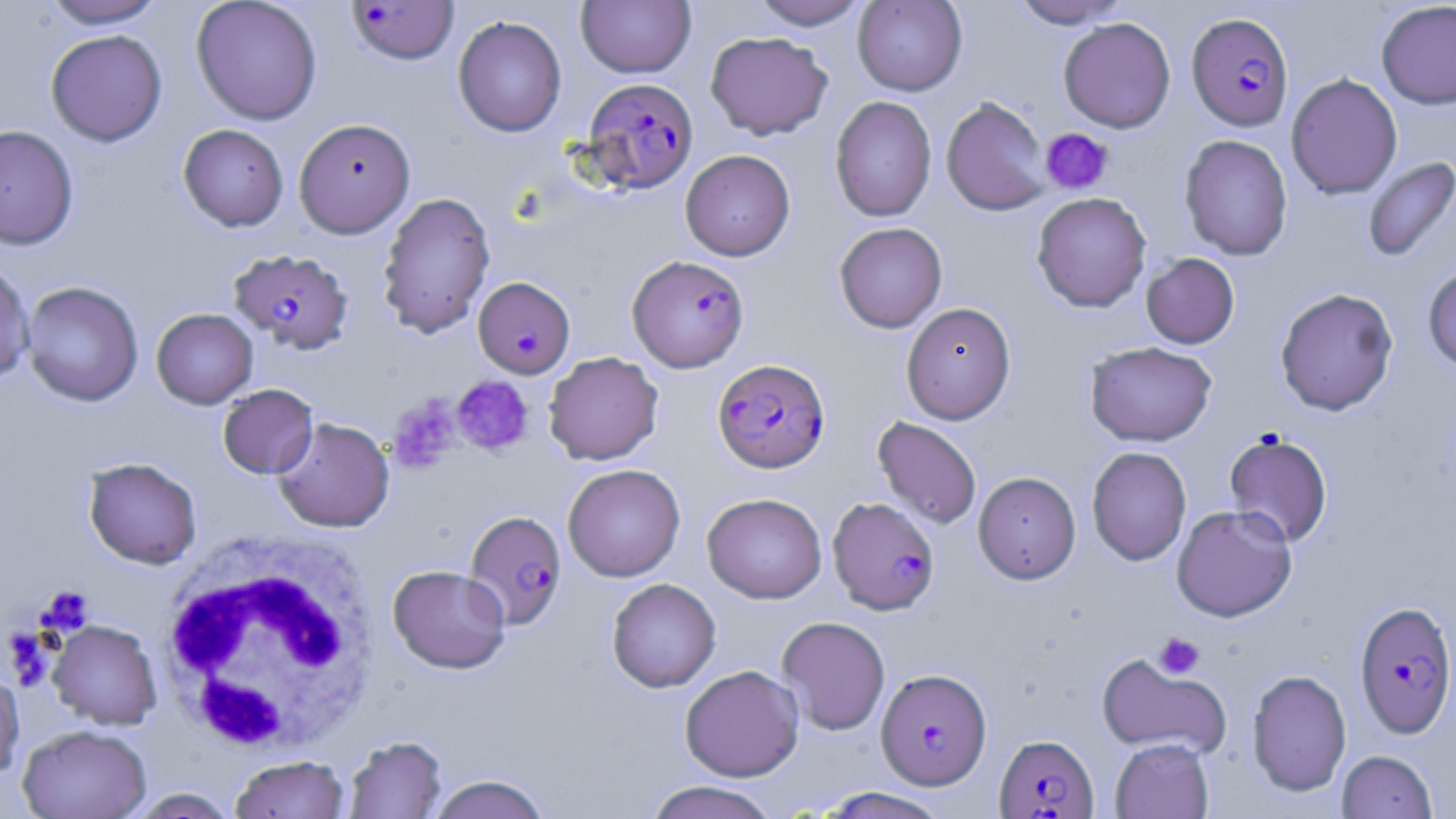

Approximate bounding boxes as named x1/y1/x2/y2 corners in pixels. White blood cell locations: (x1=156, y1=532, x2=383, y2=756). Platelet locations: (x1=1041, y1=128, x2=1113, y2=195), (x1=451, y1=375, x2=534, y2=457), (x1=391, y1=397, x2=462, y2=471), (x1=40, y1=586, x2=94, y2=634), (x1=1154, y1=633, x2=1204, y2=679). Uninfected red blood cell locations: (x1=42, y1=0, x2=168, y2=29), (x1=191, y1=0, x2=323, y2=125), (x1=749, y1=0, x2=869, y2=30), (x1=1010, y1=0, x2=1131, y2=29), (x1=576, y1=1, x2=696, y2=78), (x1=852, y1=1, x2=968, y2=96), (x1=1375, y1=1, x2=1456, y2=109), (x1=452, y1=15, x2=567, y2=137), (x1=1058, y1=17, x2=1176, y2=133), (x1=46, y1=29, x2=167, y2=146), (x1=705, y1=31, x2=833, y2=140), (x1=1285, y1=73, x2=1403, y2=200), (x1=829, y1=96, x2=937, y2=222), (x1=941, y1=96, x2=1053, y2=216), (x1=294, y1=118, x2=416, y2=238), (x1=178, y1=124, x2=289, y2=231), (x1=0, y1=125, x2=79, y2=250), (x1=1179, y1=134, x2=1293, y2=261), (x1=680, y1=149, x2=795, y2=261), (x1=1362, y1=156, x2=1456, y2=263), (x1=377, y1=191, x2=496, y2=338), (x1=1031, y1=191, x2=1151, y2=312), (x1=834, y1=223, x2=947, y2=334), (x1=1141, y1=253, x2=1240, y2=349), (x1=0, y1=260, x2=35, y2=385), (x1=1422, y1=263, x2=1456, y2=372), (x1=21, y1=280, x2=144, y2=406), (x1=1275, y1=287, x2=1399, y2=416), (x1=901, y1=302, x2=1016, y2=424), (x1=151, y1=308, x2=258, y2=409), (x1=1085, y1=341, x2=1217, y2=446), (x1=544, y1=352, x2=664, y2=465), (x1=218, y1=384, x2=318, y2=478), (x1=872, y1=416, x2=982, y2=529), (x1=272, y1=417, x2=394, y2=532), (x1=1223, y1=430, x2=1333, y2=547), (x1=1087, y1=446, x2=1191, y2=565), (x1=83, y1=457, x2=202, y2=569), (x1=562, y1=463, x2=685, y2=582), (x1=973, y1=471, x2=1081, y2=584), (x1=702, y1=493, x2=827, y2=603), (x1=1171, y1=504, x2=1297, y2=621), (x1=387, y1=564, x2=510, y2=673), (x1=607, y1=578, x2=721, y2=693), (x1=777, y1=616, x2=891, y2=735), (x1=48, y1=620, x2=162, y2=729), (x1=1096, y1=652, x2=1231, y2=759), (x1=680, y1=665, x2=804, y2=781), (x1=0, y1=669, x2=24, y2=783), (x1=1247, y1=669, x2=1351, y2=796), (x1=18, y1=724, x2=152, y2=819), (x1=342, y1=735, x2=448, y2=819), (x1=1110, y1=738, x2=1214, y2=819), (x1=1336, y1=750, x2=1438, y2=819), (x1=229, y1=755, x2=350, y2=818), (x1=426, y1=774, x2=552, y2=819), (x1=643, y1=780, x2=781, y2=819), (x1=816, y1=787, x2=953, y2=818), (x1=127, y1=788, x2=239, y2=818). Plasmodium falciparum-infected red blood cell locations: (x1=346, y1=1, x2=459, y2=66), (x1=1187, y1=12, x2=1293, y2=130), (x1=582, y1=77, x2=698, y2=194), (x1=228, y1=248, x2=354, y2=354), (x1=627, y1=255, x2=749, y2=372), (x1=473, y1=276, x2=575, y2=378), (x1=713, y1=357, x2=830, y2=472), (x1=828, y1=496, x2=940, y2=615), (x1=465, y1=511, x2=566, y2=630), (x1=1354, y1=600, x2=1456, y2=738), (x1=876, y1=668, x2=992, y2=789), (x1=994, y1=733, x2=1100, y2=817). Slide-level diagnosis: Plasmodium falciparum. Optical microscopy. Image is 1456×819 pixels. Captured at 1000x magnification. Thin blood smear. One field of a larger specimen. May-Grünwald-Giemsa stain.